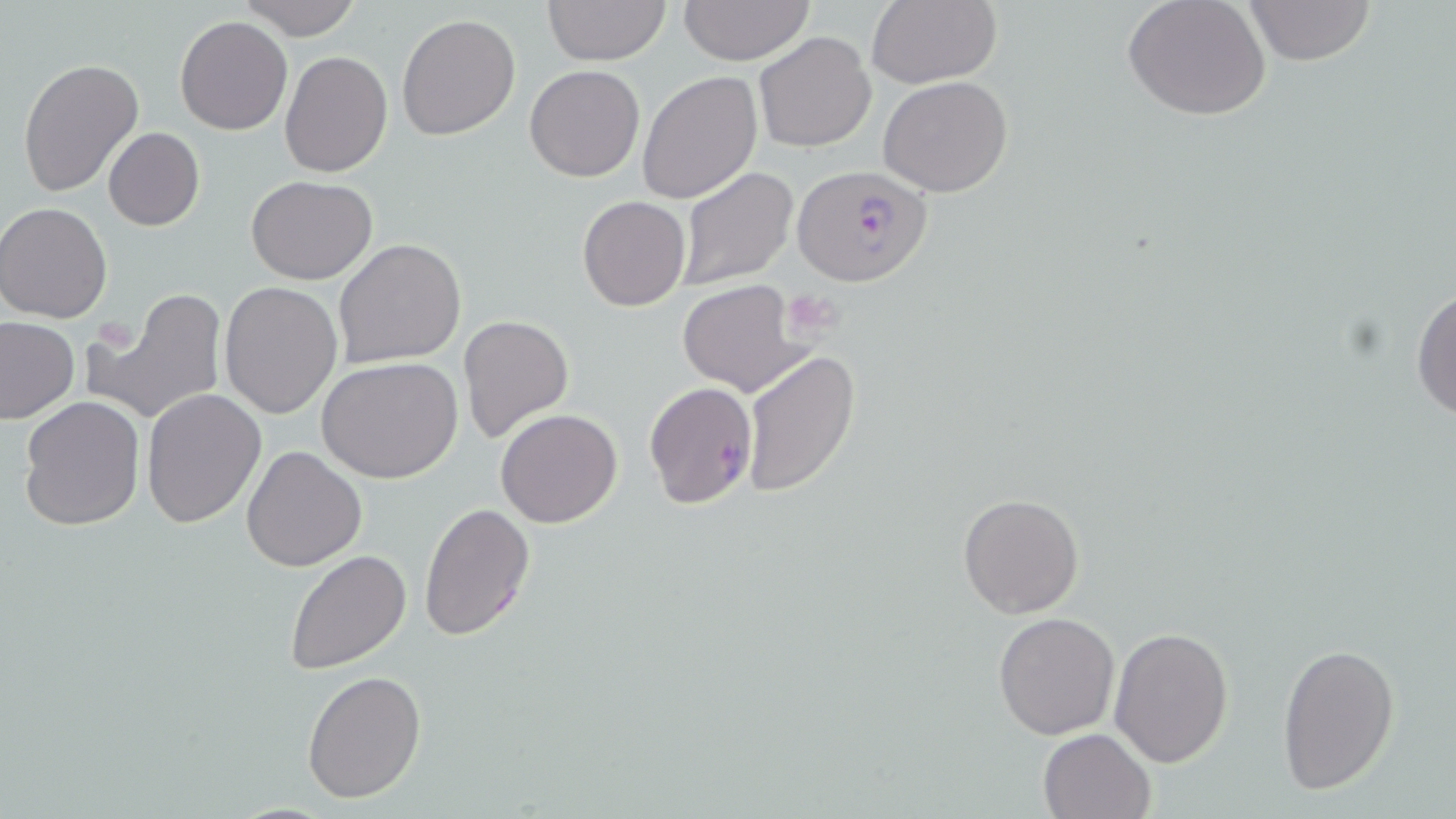
Summary:
  - Coordinate format: approximate bounding boxes as [x1, y1, x2, y2] in pixels
  - Platelet locations: [782, 291, 842, 337], [102, 323, 139, 357]
  - Plasmodium falciparum-infected red blood cell locations: [790, 163, 932, 288], [644, 381, 758, 508]
  - Uninfected red blood cell locations: [236, 0, 366, 41], [679, 0, 815, 65], [867, 0, 1002, 88], [1121, 0, 1272, 122], [1240, 0, 1378, 66], [543, 1, 669, 65], [396, 13, 521, 141], [175, 16, 292, 135], [754, 30, 876, 152], [280, 50, 393, 177], [18, 57, 144, 196], [525, 64, 644, 182], [637, 70, 763, 204], [879, 76, 1013, 197], [103, 128, 205, 231], [675, 166, 798, 291], [245, 174, 377, 284], [577, 196, 690, 311], [0, 202, 113, 323], [334, 238, 467, 370], [676, 278, 811, 396], [1412, 278, 1456, 422], [219, 282, 343, 418], [91, 288, 227, 426], [458, 314, 574, 444], [1, 318, 79, 424], [739, 347, 861, 499], [318, 357, 463, 484], [141, 388, 267, 528], [18, 396, 145, 531], [495, 409, 623, 528], [243, 445, 366, 572], [958, 493, 1084, 619], [418, 501, 536, 643], [284, 550, 412, 674], [993, 611, 1120, 739], [1109, 624, 1234, 767], [1276, 639, 1401, 793], [303, 670, 427, 804], [1038, 727, 1155, 819]
  - Slide-level diagnosis: Plasmodium falciparum
  - Magnification: 1000x
  - Stain: May-Grünwald-Giemsa
  - Preparation: thin blood film
  - Image size: 1456×819 pixels
  - Modality: optical microscopy
  - Field of view: single